Comment on the morphology of the erythrocytes.
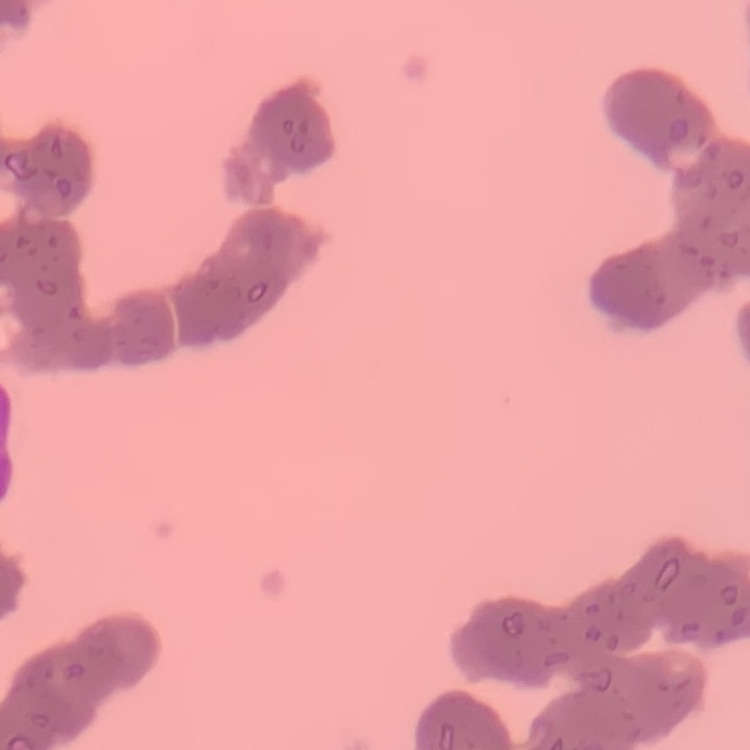

Rouleaux formation.

{
  "image_type": "square crop of a larger photomicrograph",
  "stain": "Field's or Giemsa",
  "preparation": "thin blood film"
}